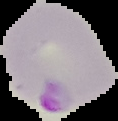 Malaria status: parasitized. Image is 118×121 pixels. From a thin blood smear. The area outside the segmented cell region is set to black.